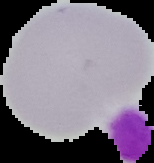
result: negative for Plasmodium parasites
image_type: cell region segmented out of the field of view; surrounding area masked to black
preparation: thin blood film
image_size: 154×163 pixels